Describe the morphology of the red blood cells.
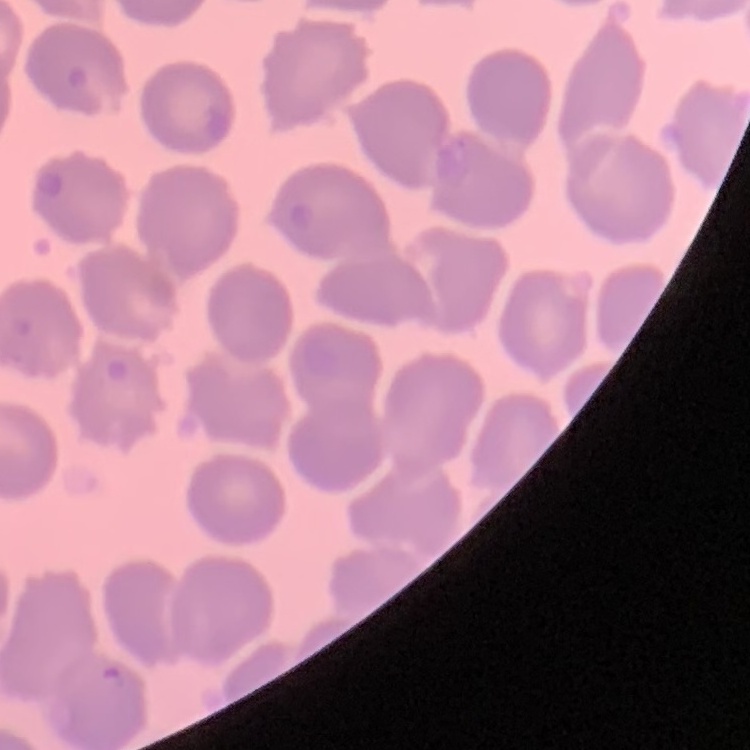
They show no rouleaux formation.

stain: Field's or Giemsa
image_type: one tile cut from a larger photomicrograph
preparation: thin blood smear